Identify the parasite.
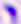
This is Toxoplasma gondii.

Summary:
  - Modality: micrograph
  - Magnification: 400x